Report the malaria status of this cell.
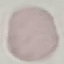

Uninfected.

image_type: automatically extracted cell patch, resized to 64 × 64 pixels
preparation: thin blood smear
capture: smartphone through the microscope eyepiece
stain: Giemsa